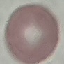
Summary:
  - Malaria status: uninfected
  - Preparation: thin smear
  - Capture: smartphone through the microscope eyepiece
  - Image type: automatically extracted cell patch, resized to 64 × 64 pixels
  - Stain: Giemsa